Give a bounding box for every artifact (platelet-like body, stain precipitate, or debris).
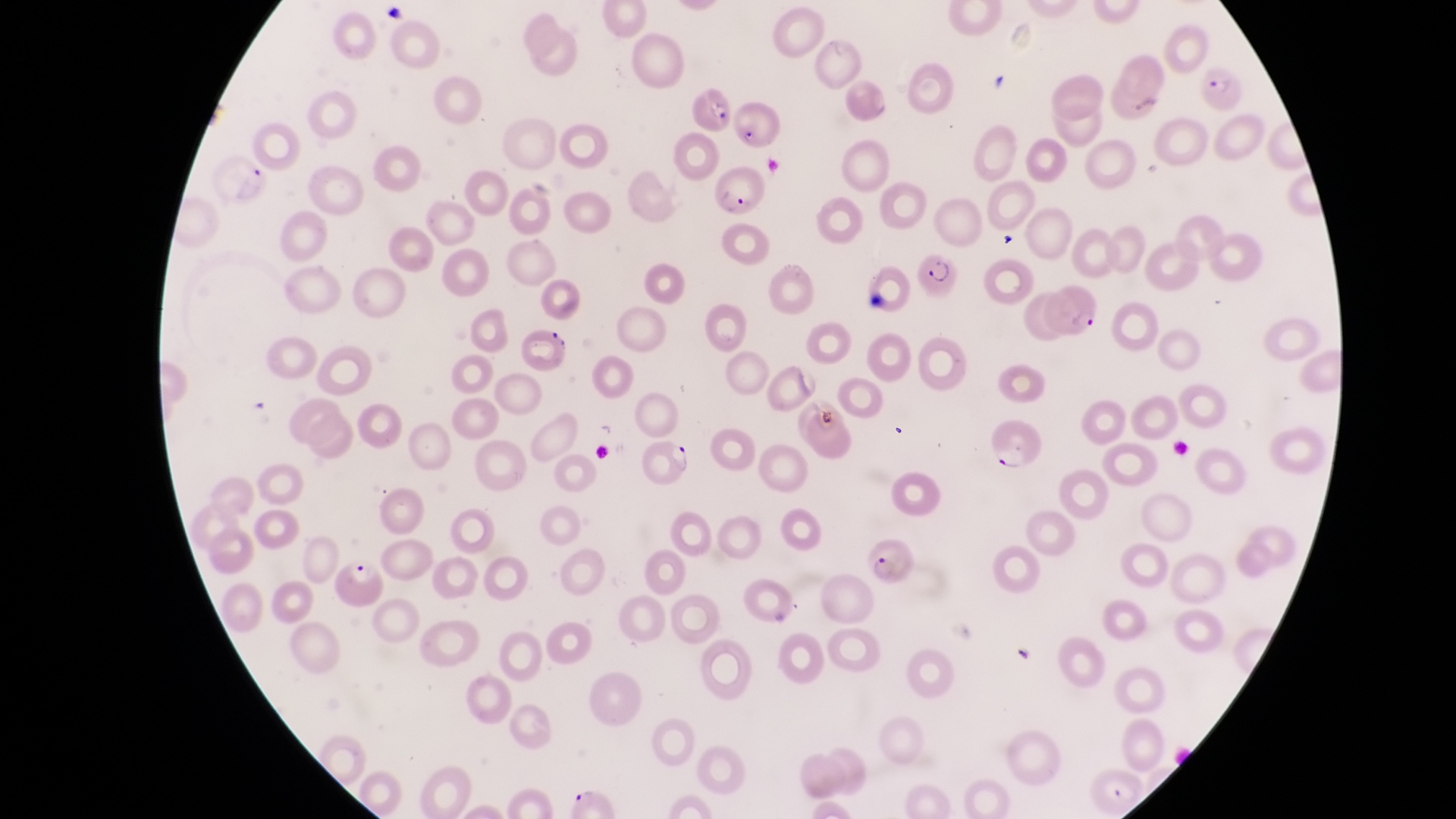
Approximate bounding boxes as [left, top, right, bottom] in pixels.
Artifacts (platelet-like body, stain precipitate, or debris): [544, 328, 574, 352].

Parasitised red blood cell locations: [1195, 71, 1250, 117], [690, 86, 732, 132], [730, 95, 780, 151], [211, 155, 266, 207], [716, 171, 768, 220], [918, 243, 961, 302], [1046, 283, 1104, 342], [987, 417, 1042, 475], [632, 436, 693, 492], [864, 539, 920, 589]. Thin blood smear. Captured by a smartphone held over the eyepiece of an Olympus CX-23 microscope. Magnification of 1000x. Single field of view. Collected in Uganda. Image is 1456×819 pixels.